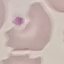
malaria_status: uninfected
capture: smartphone camera at the microscope eyepiece
stain: Giemsa
preparation: thin blood smear
image_type: automatically extracted cell patch, resized to 64 × 64 pixels